Give the preparation type.
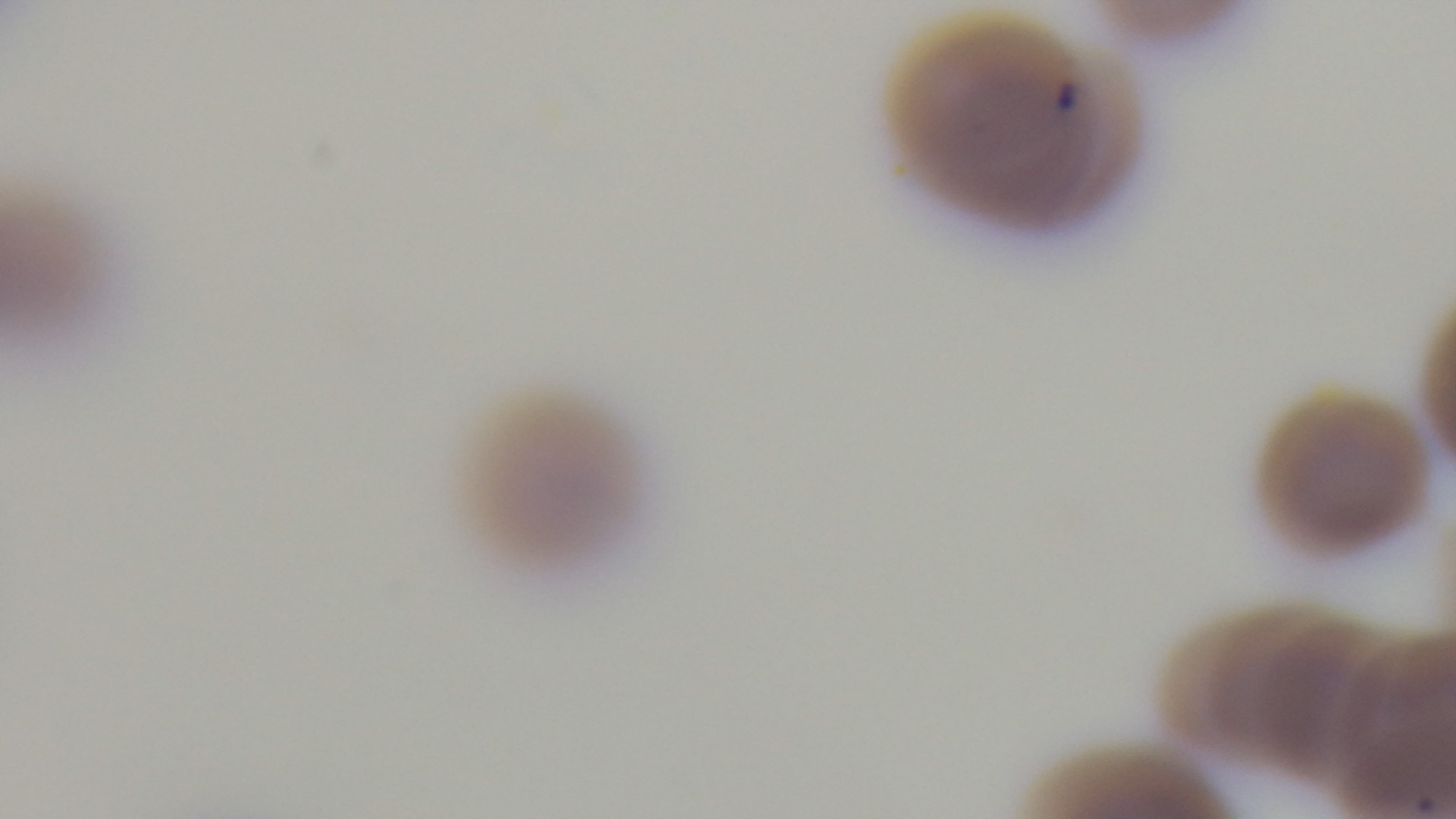
Thin.

Mounted 4K digital camera. Oil-immersion objective, 100x. Malaria status: infected. One field from the slide. Photomicrograph. Giemsa-stained.